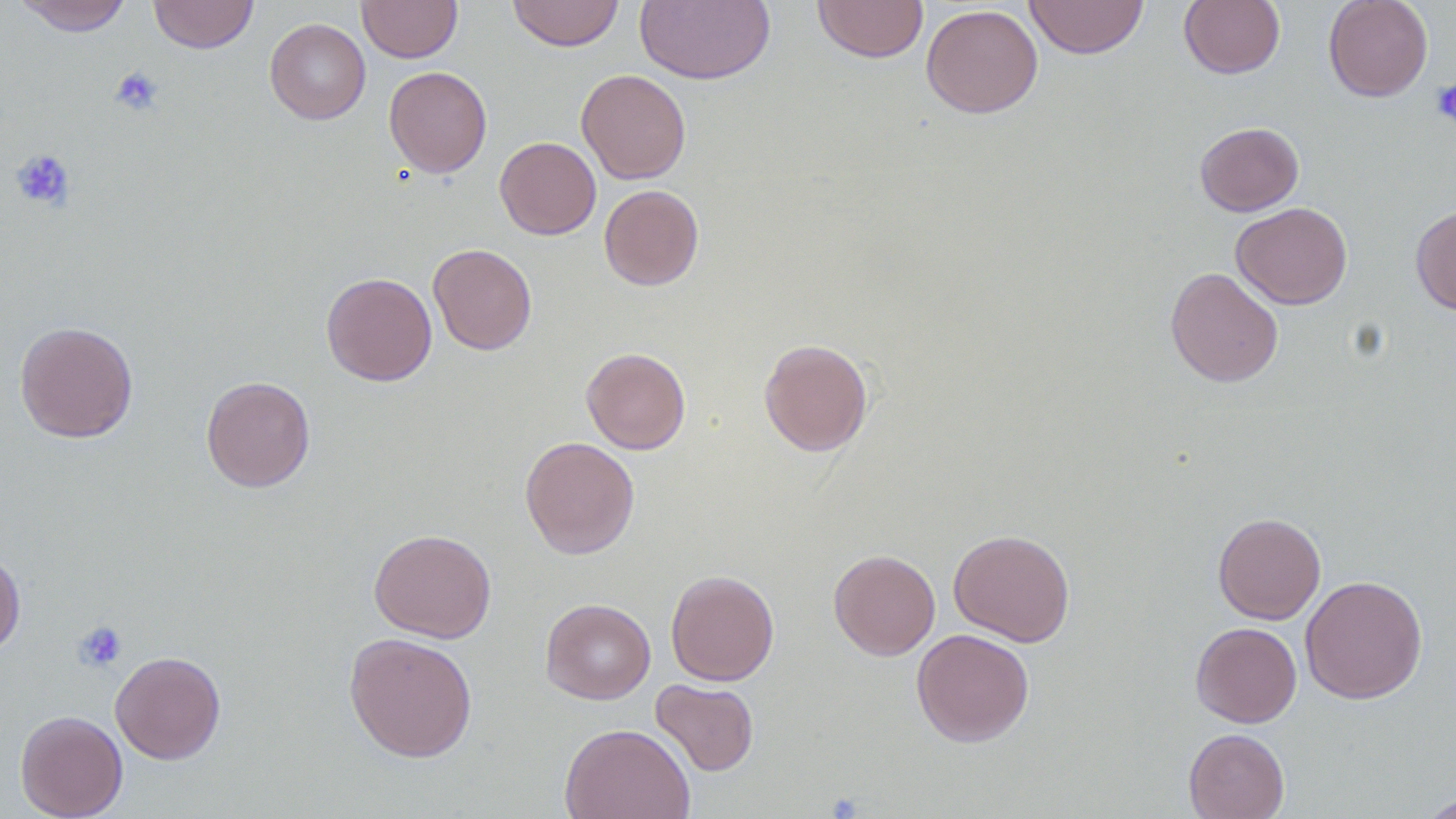

Summary:
  - Coordinate format: approximate bounding boxes as (x1,y1)-(x2,y2) corner pairs in pixels
  - Uninfected red blood cell locations: (14,0)-(132,36), (149,0)-(258,54), (357,0)-(462,63), (507,0)-(625,51), (635,0)-(776,85), (812,0)-(929,63), (1024,0)-(1149,59), (1179,0)-(1285,79), (1323,0)-(1433,102), (921,4)-(1043,118), (264,18)-(371,124), (384,66)-(492,177), (576,68)-(691,184), (1194,122)-(1304,216), (495,136)-(601,240), (599,184)-(704,291), (1231,202)-(1353,310), (1410,205)-(1456,315), (428,243)-(537,355), (1164,267)-(1284,387), (321,272)-(437,386), (14,321)-(139,443), (759,338)-(873,456), (581,347)-(691,454), (201,376)-(315,492), (520,436)-(640,559), (1213,512)-(1326,624), (368,528)-(496,643), (948,529)-(1075,647), (828,549)-(940,660), (0,550)-(26,656), (665,569)-(779,686), (1300,574)-(1428,704), (540,598)-(656,704), (1190,622)-(1302,727), (911,628)-(1034,747), (343,631)-(478,762), (110,650)-(226,764), (651,679)-(759,776), (15,710)-(128,818), (559,722)-(696,819), (1184,728)-(1290,819), (1418,792)-(1456,819)
  - Platelet locations: (109,66)-(164,116), (1432,79)-(1456,128), (11,149)-(76,211), (73,621)-(127,672)
  - Slide-level diagnosis: negative for blood parasites
  - Magnification: 1000x
  - Modality: optical microscopy
  - Field of view: single
  - Preparation: thin blood smear
  - Image size: 1456×819 pixels